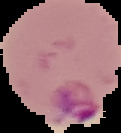
From a thin blood smear. Malaria status: parasitized. Image is 121×133 pixels. Segmented cell region on a black background.